Locate and identify every blood parasite.
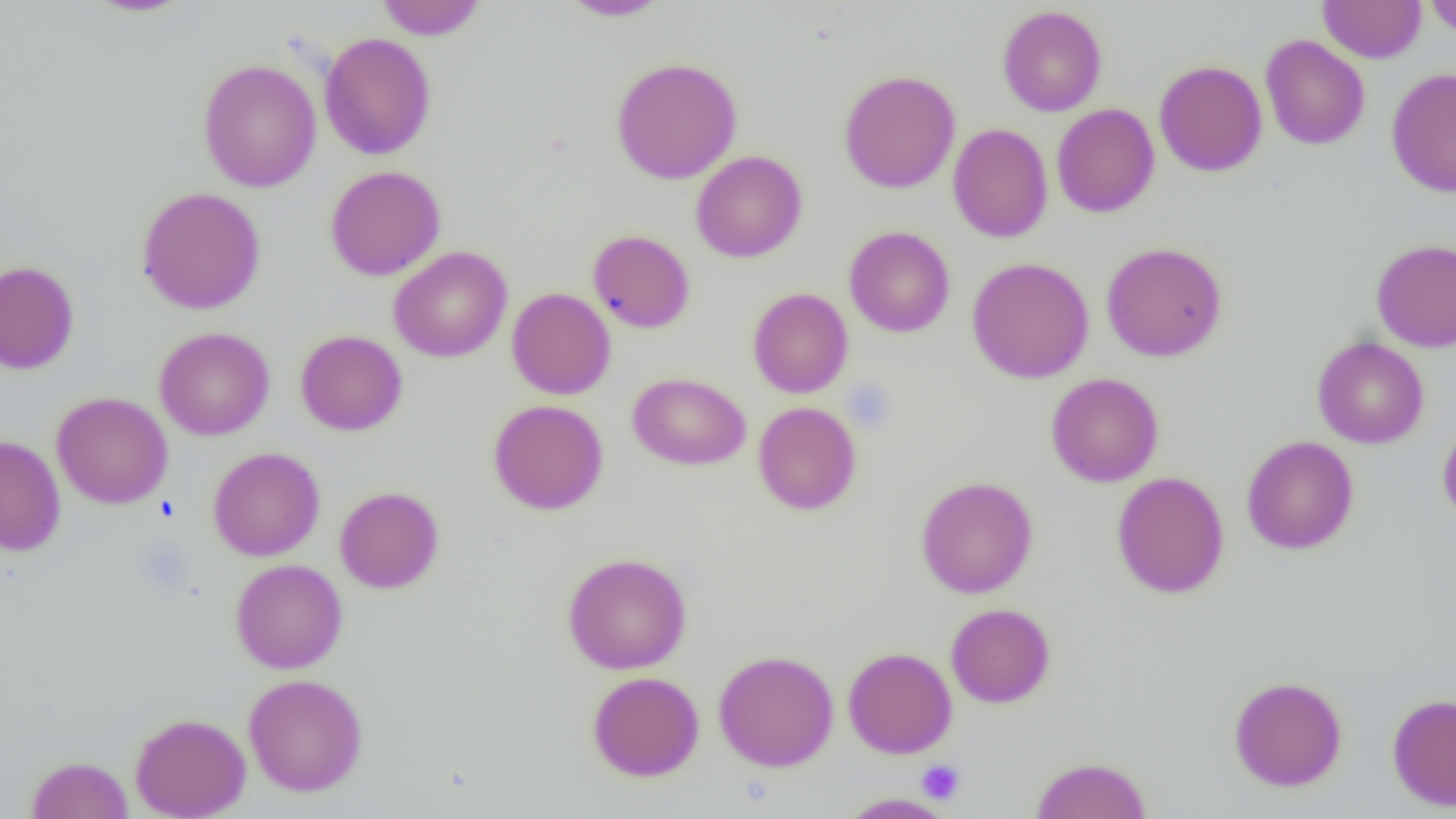
No blood parasites seen.

Summary:
  - Coordinate format: approximate bounding boxes as (x1,y1)-(x2,y2) corner pairs in pixels
  - Platelet locations: (842,378)-(898,434), (917,759)-(965,805)
  - Uninfected red blood cell locations: (84,0)-(195,17), (375,0)-(487,40), (560,0)-(672,21), (1318,0)-(1425,63), (1424,0)-(1456,38), (997,5)-(1107,116), (319,32)-(437,160), (1260,35)-(1370,150), (611,57)-(742,184), (197,59)-(322,193), (1154,60)-(1267,177), (1386,68)-(1456,197), (839,69)-(961,194), (1052,103)-(1159,218), (947,118)-(1158,229), (948,123)-(1053,242), (691,150)-(807,263), (325,165)-(445,281), (136,186)-(266,314), (844,226)-(955,338), (588,229)-(695,333), (1371,239)-(1456,353), (1101,242)-(1227,361), (389,246)-(512,362), (967,257)-(1094,383), (0,261)-(79,373), (507,287)-(616,400), (747,288)-(853,398), (154,327)-(275,441), (295,330)-(408,436), (1312,336)-(1429,448), (628,372)-(750,470), (1045,372)-(1164,487), (51,392)-(173,509), (488,399)-(608,515), (752,401)-(862,515), (1437,420)-(1456,525), (0,435)-(66,556), (1241,435)-(1359,555), (208,447)-(325,561), (1112,472)-(1229,598), (915,476)-(1038,598), (335,486)-(444,593), (563,552)-(692,674), (231,558)-(348,674), (945,603)-(1055,708), (843,647)-(957,758), (713,650)-(839,771), (588,672)-(704,781), (243,674)-(368,797), (1228,675)-(1347,792), (1387,693)-(1456,811), (130,712)-(251,818), (27,755)-(133,818), (1031,756)-(1151,819), (837,792)-(956,818)
  - Slide-level diagnosis: negative for blood parasites
  - Modality: optical microscopy
  - Preparation: thin blood film
  - Magnification: 1000x
  - Field of view: one of a larger specimen
  - Image size: 1456×819 pixels